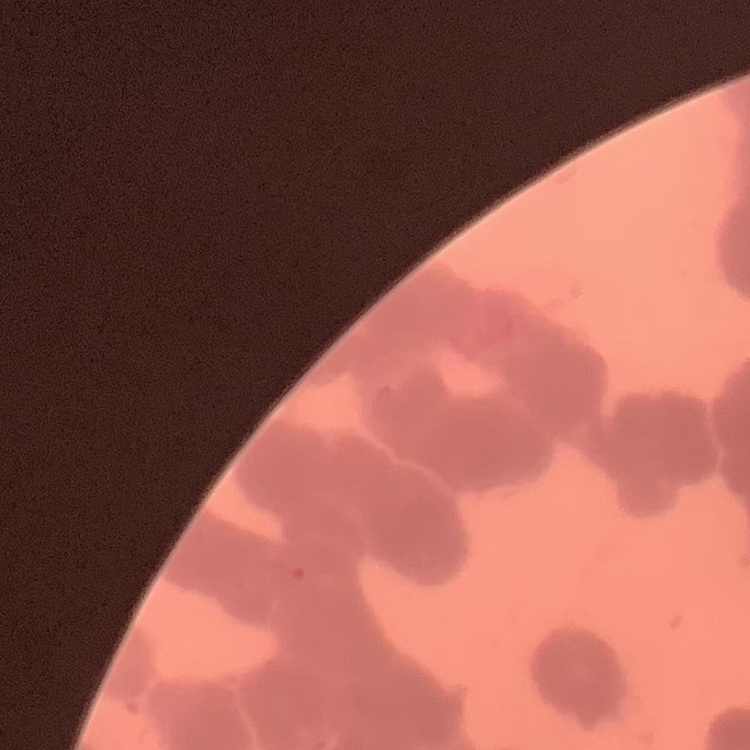

red blood cell morphology = rouleaux formation
preparation = thin blood film
stain = Field's or Giemsa
image type = one tile cut from a larger photomicrograph